Name the parasite shown.
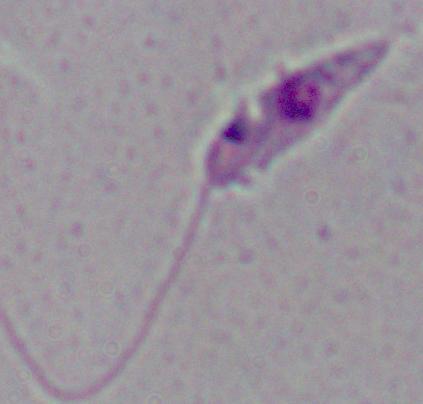
Leishmania.

Captured at 1000x magnification. Photomicrograph.